Describe the morphology of the erythrocytes.
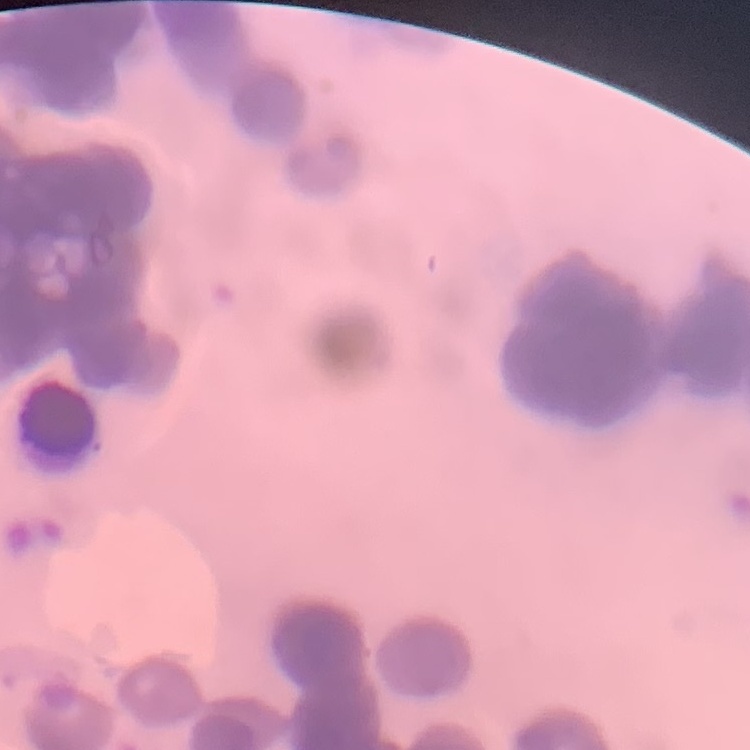

They show rouleaux formation.

Summary:
  - Stain: Field's or Giemsa
  - Image type: one tile cut from a larger photomicrograph
  - Preparation: thin peripheral smear